Point out each leukocyte.
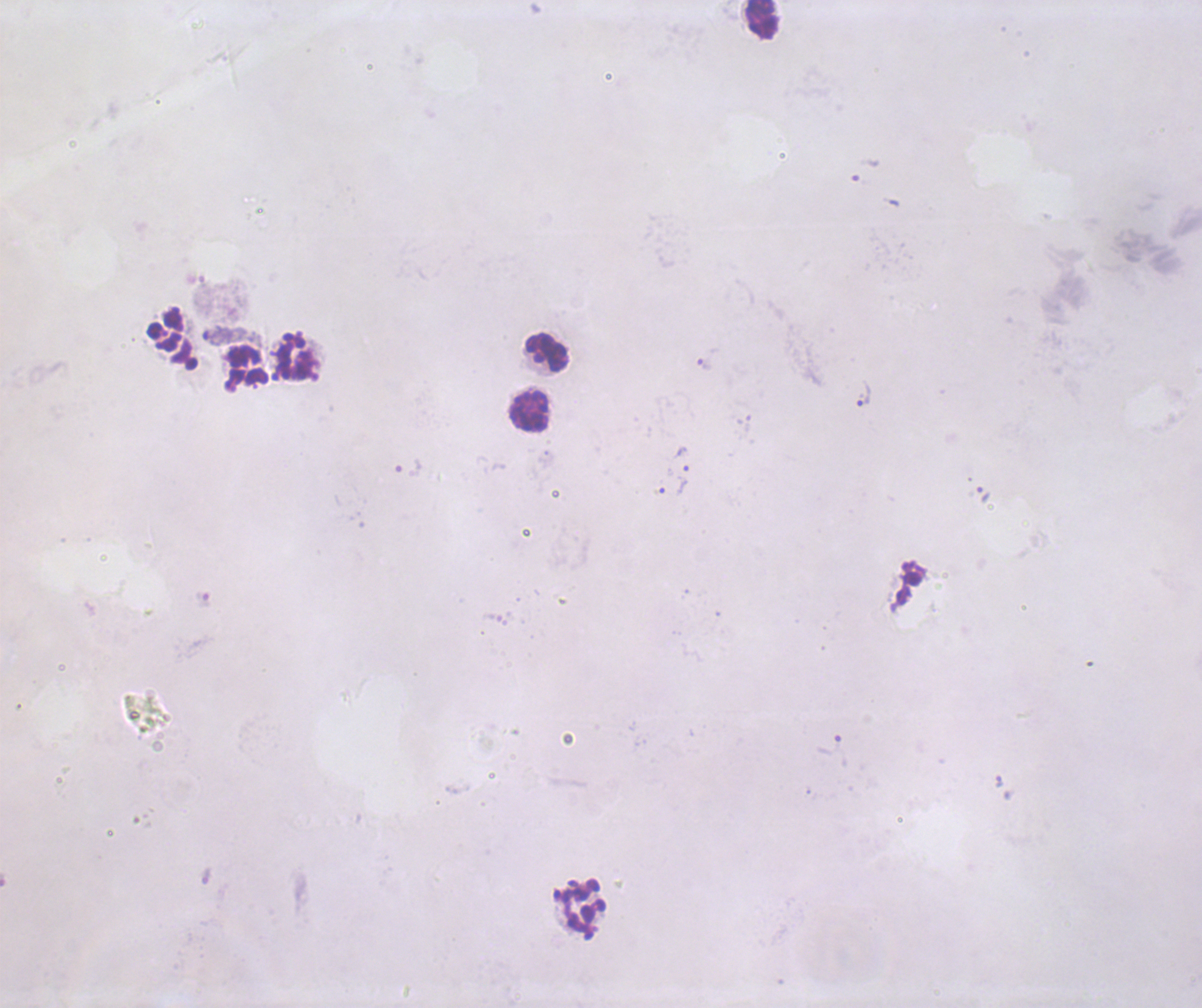
Approximate object centers, in pixels from the top-left corner.
Leukocytes: (x=761, y=19), (x=546, y=352), (x=294, y=358), (x=248, y=366), (x=529, y=412), (x=584, y=907).

Approximate object centers, in pixels from the top-left corner. Trophozoite locations: (x=708, y=360), (x=863, y=393), (x=682, y=458), (x=673, y=487), (x=984, y=494), (x=829, y=744), (x=999, y=782). Result: malaria parasites identified. Previously used in an actual diagnosis. 100x magnification. Coloration quality: bad. Image is 1202×1008 pixels. Thick blood film. Background quality: unsatisfactory. Romanowsky stain. One field from this slide.